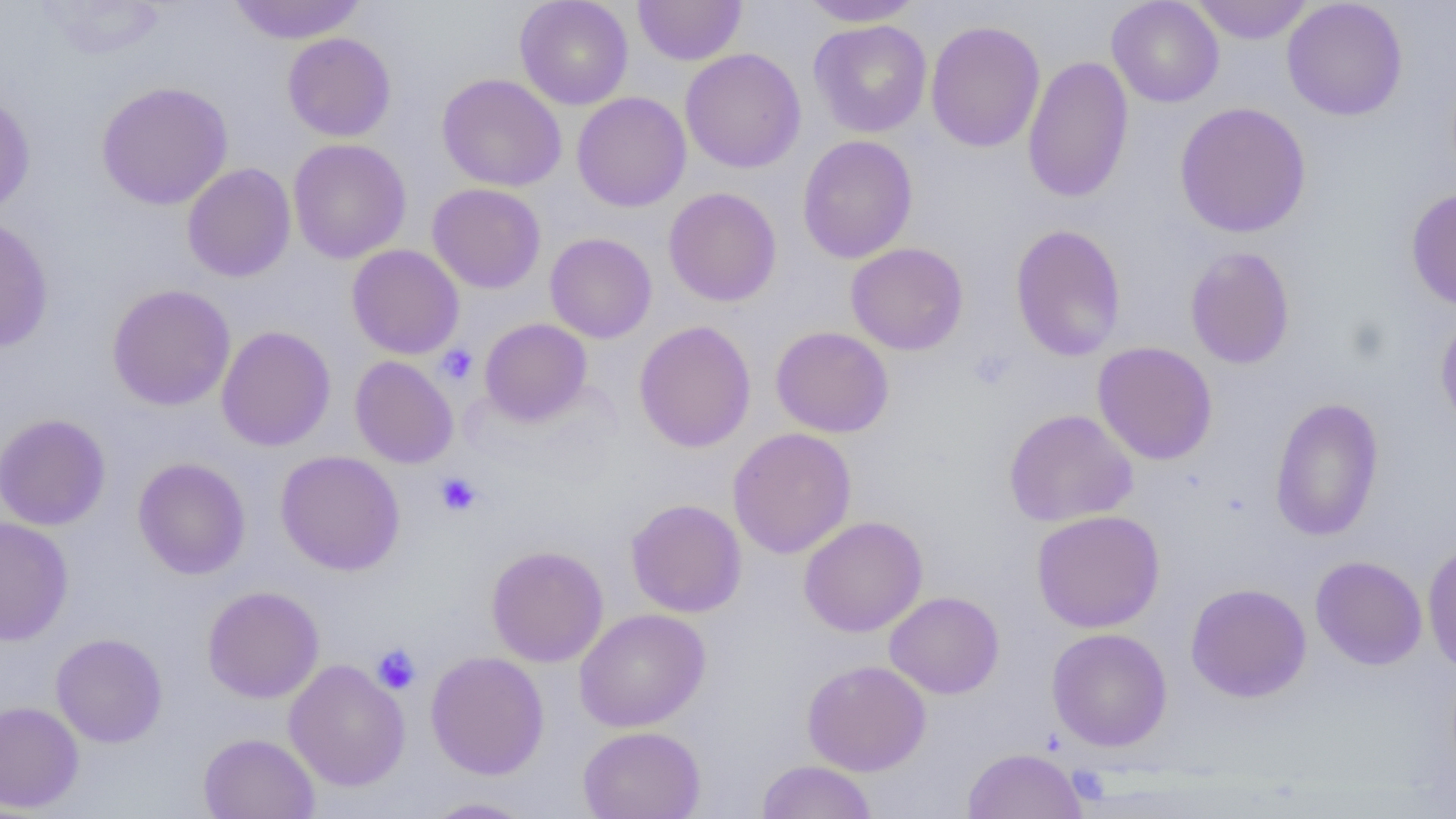

Summary:
  - Coordinate format: approximate bounding boxes as (x1,y1)-(x2,y2) corner pairs in pixels
  - Platelet locations: (436,344)-(477,385), (969,348)-(1016,391), (435,472)-(482,516), (371,644)-(422,694)
  - Uninfected red blood cell locations: (33,0)-(167,59), (227,0)-(367,44), (515,0)-(634,110), (633,0)-(747,65), (796,0)-(926,27), (1107,0)-(1224,108), (1190,0)-(1314,44), (1282,0)-(1408,121), (809,19)-(932,137), (925,20)-(1045,153), (282,32)-(397,142), (680,48)-(806,173), (1022,56)-(1134,203), (437,73)-(567,192), (96,80)-(234,210), (0,90)-(36,217), (572,92)-(691,212), (1173,102)-(1312,238), (797,134)-(918,264), (287,138)-(412,264), (182,162)-(296,282), (427,183)-(546,293), (663,187)-(782,307), (1405,188)-(1456,311), (0,214)-(54,353), (1010,224)-(1127,362), (544,232)-(657,343), (846,242)-(969,355), (346,244)-(464,359), (1185,246)-(1295,370), (107,283)-(236,411), (1434,311)-(1456,435), (479,318)-(592,426), (633,320)-(756,452), (216,325)-(336,451), (770,326)-(894,438), (1092,341)-(1218,465), (349,356)-(458,468), (1269,397)-(1384,541), (1004,408)-(1138,527), (0,413)-(111,531), (727,427)-(857,559), (276,450)-(405,576), (133,457)-(251,579), (626,499)-(747,617), (1031,510)-(1165,633), (799,515)-(927,637), (0,516)-(74,645), (1422,539)-(1456,674), (486,545)-(609,667), (1310,555)-(1427,670), (1185,583)-(1312,703), (202,585)-(325,703), (884,590)-(1004,699), (574,608)-(711,732), (1046,627)-(1172,752), (50,632)-(168,748), (426,651)-(550,780), (284,659)-(410,791), (802,659)-(931,776), (0,701)-(84,812), (577,725)-(706,819), (198,732)-(320,819), (962,747)-(1088,819), (757,760)-(877,819), (420,796)-(538,818)
  - Slide-level diagnosis: no evidence of blood parasites
  - Preparation: thin blood smear
  - Field of view: one of a larger specimen
  - Magnification: 1000x
  - Modality: optical microscopy
  - Image size: 1456×819 pixels